Name the cell type shown.
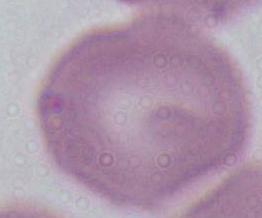

An erythrocyte.

Captured at 1000x magnification. Micrograph.